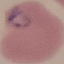

{
  "result": "malaria parasites identified",
  "image_type": "cell patch, automatically extracted from a larger field of view and resized to 64 × 64 pixels",
  "stain": "Giemsa",
  "capture": "smartphone camera at the microscope eyepiece",
  "preparation": "thin blood film"
}